Classify this cell by malaria status.
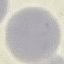

Uninfected.

Summary:
  - Image type: automatically extracted cell patch, resized to 64 × 64 pixels
  - Capture: smartphone through the microscope eyepiece
  - Stain: Giemsa
  - Preparation: thin blood film